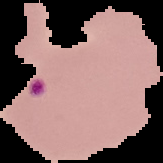

preparation = thin blood film
result = malaria parasites detected
image type = segmented cell region on a black background
image size = 163×163 pixels